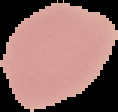

Malaria status: uninfected. From a thin blood smear. The area outside the segmented cell region is set to black. Image is 118×112 pixels.